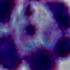

A leukocyte is shown. 1000x magnification. Micrograph.